Comment on the morphology of the erythrocytes.
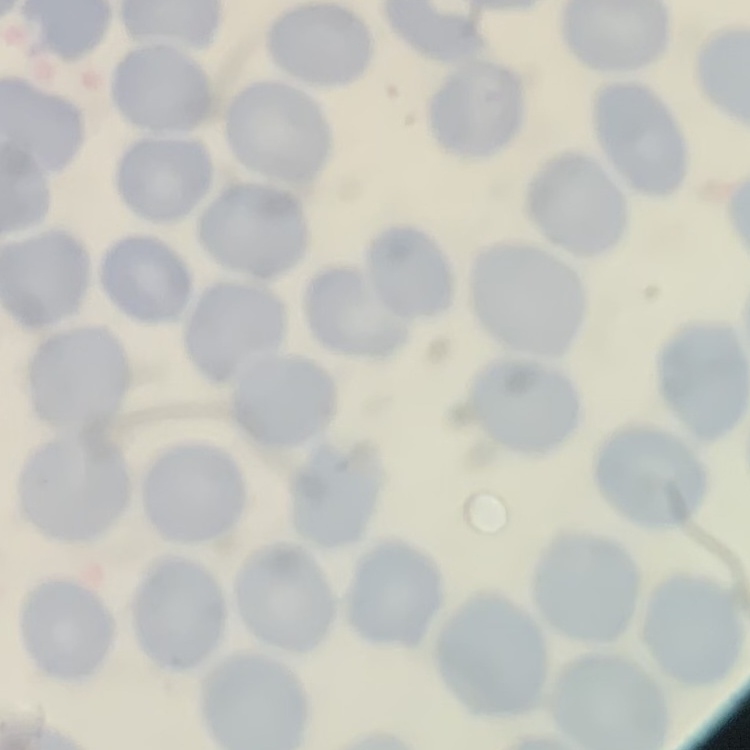

They show no rouleaux formation.

Thin blood smear. Stained with either Field's or Giemsa. Square crop of a larger photomicrograph.